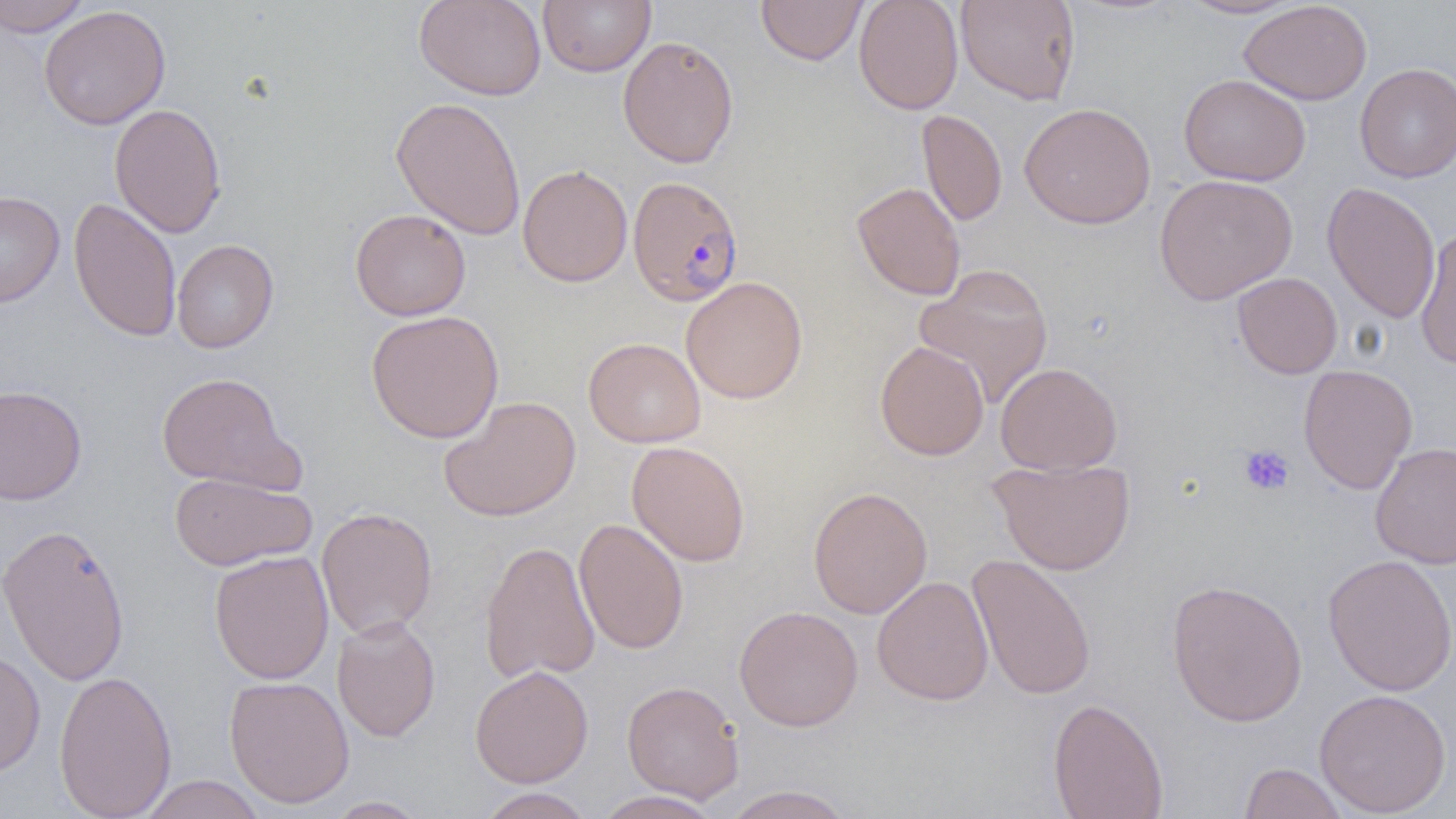 Approximate bounding boxes as [x1, y1, x2, y2] in pixels. Platelet locations: [1239, 444, 1295, 496]. Plasmodium falciparum-infected red blood cell locations: [627, 175, 744, 307]. Uninfected red blood cell locations: [0, 0, 93, 37], [414, 0, 547, 101], [538, 0, 655, 77], [756, 0, 868, 66], [854, 0, 963, 114], [956, 0, 1080, 105], [1177, 0, 1304, 19], [1239, 1, 1373, 105], [39, 5, 171, 130], [617, 35, 739, 168], [1354, 62, 1456, 183], [1179, 73, 1311, 187], [390, 96, 526, 240], [1019, 102, 1157, 229], [109, 103, 226, 238], [917, 109, 1007, 226], [517, 164, 633, 287], [1154, 174, 1298, 304], [852, 181, 966, 301], [1322, 181, 1441, 323], [0, 190, 65, 309], [68, 196, 182, 343], [350, 209, 471, 321], [1414, 226, 1456, 371], [172, 239, 278, 353], [913, 263, 1054, 408], [1232, 272, 1342, 379], [681, 276, 808, 404], [366, 310, 504, 443], [584, 337, 706, 448], [875, 340, 989, 461], [995, 362, 1122, 476], [1298, 364, 1417, 494], [156, 371, 300, 492], [0, 384, 87, 506], [439, 396, 581, 522], [626, 440, 751, 566], [1370, 441, 1456, 570], [989, 458, 1135, 575], [168, 472, 316, 571], [808, 486, 932, 619], [316, 506, 438, 640], [574, 518, 689, 655], [0, 522, 131, 687], [479, 540, 601, 684], [209, 550, 334, 684], [967, 553, 1097, 701], [1323, 554, 1456, 697], [872, 575, 994, 706], [1166, 579, 1308, 727], [734, 605, 863, 732], [332, 615, 441, 742], [0, 648, 46, 777], [469, 664, 594, 788], [53, 669, 177, 819], [224, 675, 355, 808], [622, 680, 744, 803], [1313, 688, 1452, 817], [1048, 697, 1168, 819], [1238, 762, 1350, 819], [138, 775, 267, 818], [721, 785, 857, 818], [476, 788, 594, 819], [593, 790, 723, 819], [324, 796, 431, 818]. Slide-level diagnosis: Plasmodium falciparum. Single field of view. Captured at 1000x magnification. Thin blood smear. Light microscopy. Image is 1456×819 pixels.